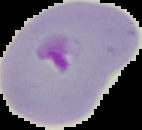
result: Plasmodium parasites identified
image_type: cell region segmented out of the field of view; surrounding area masked to black
preparation: thin blood smear
image_size: 142×130 pixels